Comment on the morphology of the red blood cells.
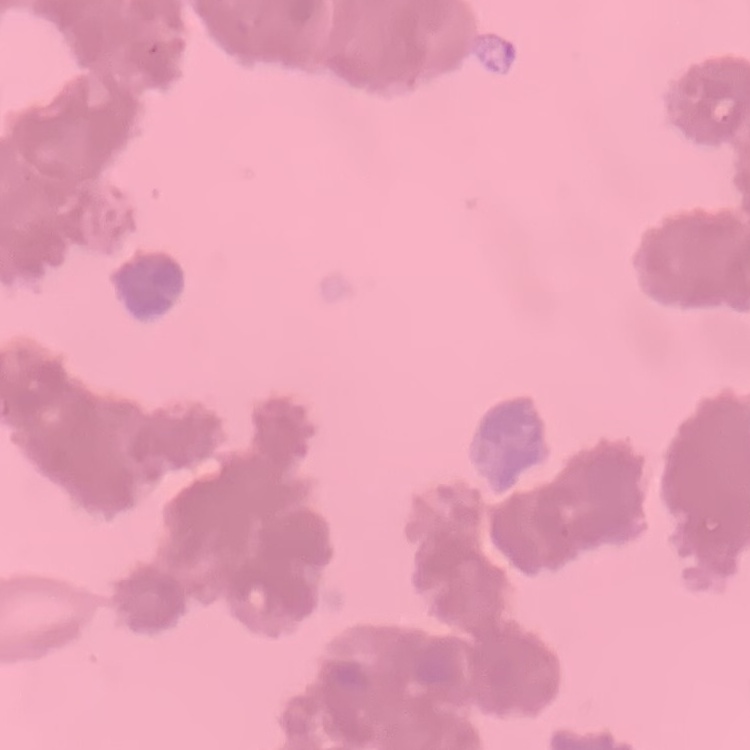

Rouleaux formation.

Summary:
  - Stain: Field's or Giemsa
  - Preparation: thin peripheral smear
  - Image type: square crop of a larger photomicrograph